State the blood parasite species.
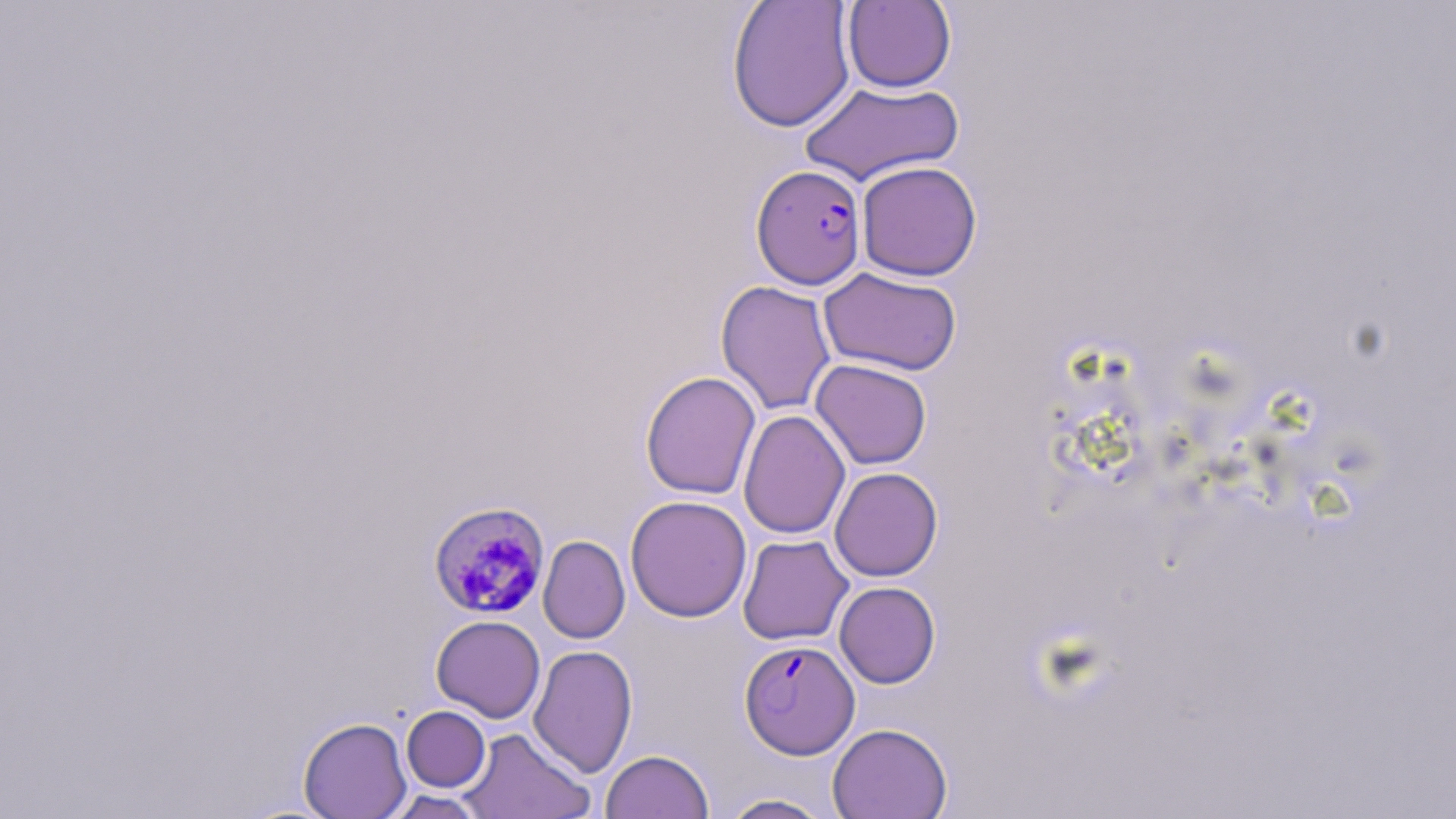
Plasmodium falciparum.

Approximate bounding boxes as (x1,y1)-(x2,y2) corner pairs in pixels. Uninfected red blood cell locations (subset): (726,0)-(856,132), (842,1)-(956,93), (799,79)-(964,187), (856,161)-(982,281), (818,267)-(962,376), (715,280)-(836,416), (810,358)-(932,470), (640,371)-(761,500), (738,409)-(850,540), (829,467)-(943,581), (625,495)-(752,622), (737,534)-(853,645), (538,536)-(630,643), (834,581)-(940,688), (431,615)-(546,723), (528,645)-(638,778), (401,706)-(490,792), (298,716)-(412,818), (827,723)-(953,819), (458,727)-(595,819), (600,750)-(714,819), (383,790)-(489,818), (718,793)-(835,818). Plasmodium falciparum-infected red blood cell locations (subset): (751,165)-(867,289), (428,500)-(550,624). Image is 1456×819 pixels. Thin blood smear. 1000x magnification. Light microscopy. One field of a larger specimen. May-Grünwald-Giemsa-stained preparation.